Locate every Trypanosoma brucei.
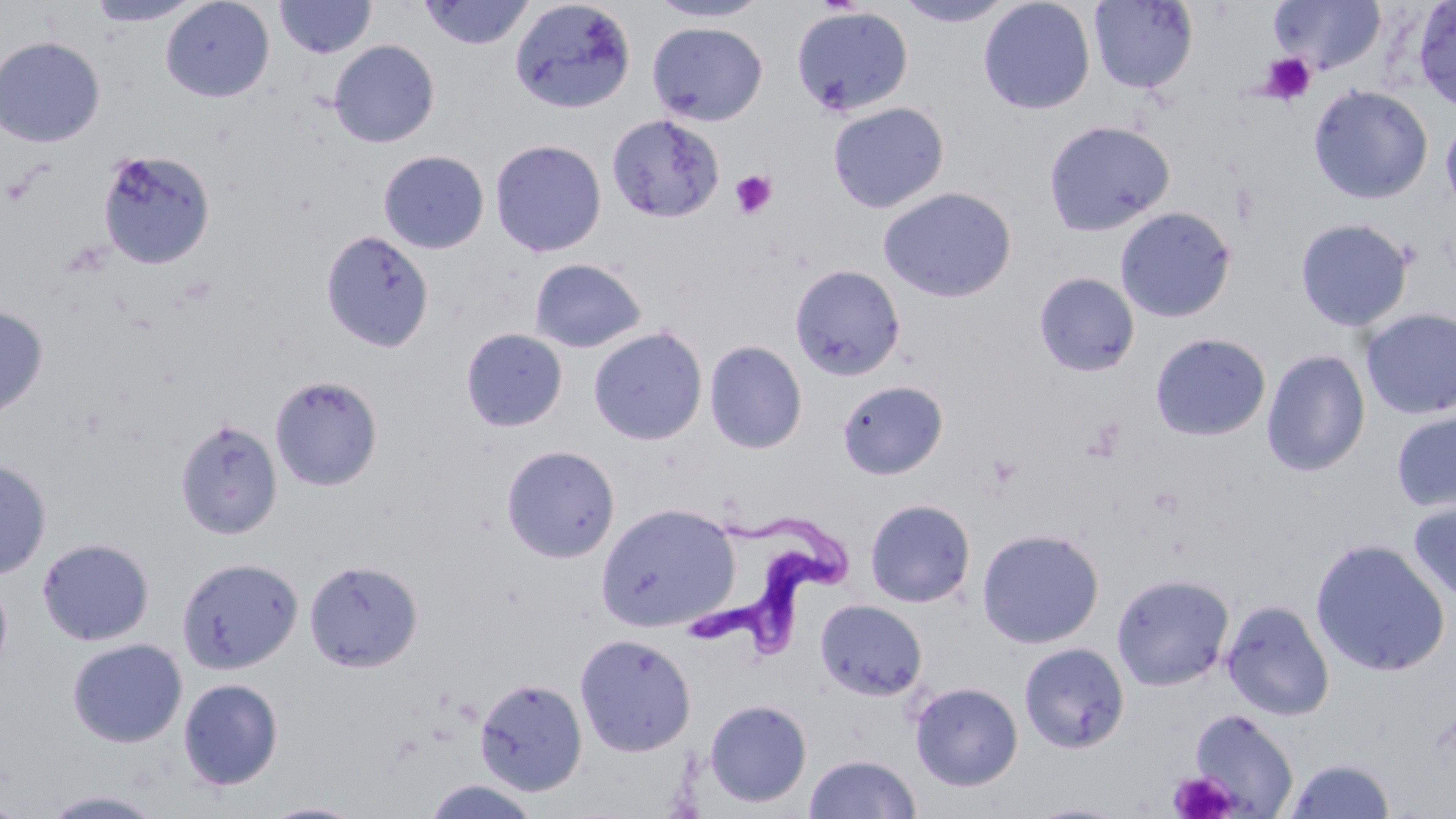
Approximate bounding boxes as (x1,y1)-(x2,y2) corner pairs in pixels.
Trypanosoma brucei: (690,499)-(845,655).

Uninfected red blood cell locations: (160,0)-(275,102), (274,0)-(377,59), (509,0)-(637,114), (645,0)-(774,23), (978,0)-(1096,115), (1088,0)-(1198,94), (1268,0)-(1385,74), (84,1)-(206,27), (419,1)-(535,50), (894,1)-(1017,28), (1411,1)-(1456,113), (790,5)-(915,117), (647,21)-(769,126), (0,36)-(105,147), (329,39)-(440,148), (1308,84)-(1433,205), (827,101)-(949,213), (606,113)-(725,223), (1440,114)-(1456,218), (1042,119)-(1175,236), (490,139)-(607,257), (97,149)-(216,270), (378,150)-(489,254), (878,186)-(1017,303), (1114,205)-(1236,323), (1294,217)-(1414,332), (320,230)-(434,353), (529,258)-(647,354), (789,264)-(905,381), (1034,272)-(1140,377), (0,304)-(48,418), (1360,307)-(1456,420), (588,327)-(708,445), (461,328)-(568,433), (1150,332)-(1271,441), (704,340)-(807,454), (1261,348)-(1371,477), (270,375)-(383,491), (837,380)-(948,480), (1390,409)-(1456,514), (174,417)-(283,540), (501,444)-(620,563), (0,458)-(52,581), (1407,496)-(1456,605), (864,498)-(976,608), (595,501)-(741,633), (976,527)-(1104,648), (37,537)-(155,646), (1310,538)-(1451,677), (176,555)-(303,674), (304,559)-(423,672), (0,572)-(13,683), (1111,572)-(1234,691), (815,599)-(927,701), (1221,599)-(1335,721), (574,633)-(696,757), (67,638)-(187,748), (1018,641)-(1129,753), (474,677)-(587,797), (178,678)-(284,791), (910,681)-(1023,791), (703,699)-(812,808), (1188,709)-(1298,817), (804,753)-(921,819), (1284,757)-(1395,818), (422,778)-(540,818), (39,788)-(168,818), (258,800)-(372,818), (1024,800)-(1135,818). Platelet locations: (1259,53)-(1317,105), (729,169)-(778,220), (1082,417)-(1127,462), (1168,771)-(1238,819). Slide-level diagnosis: Trypanosoma brucei. Image is 1456×819 pixels. Optical microscopy. Single field of view. Thin blood smear. May-Grünwald-Giemsa stain. 1000x magnification.